State which cell type is depicted.
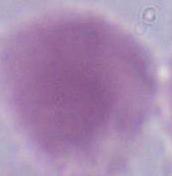

An erythrocyte.

Summary:
  - Magnification: 1000x
  - Modality: photomicrograph